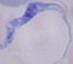
Summary:
  - Modality: micrograph
  - Magnification: 1000x
  - Identification: trypanosome